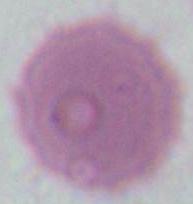 An erythrocyte is shown. Captured at 1000x magnification. Micrograph.